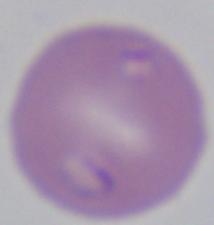 Captured at 1000x magnification. Micrograph. A Babesia parasite is shown.